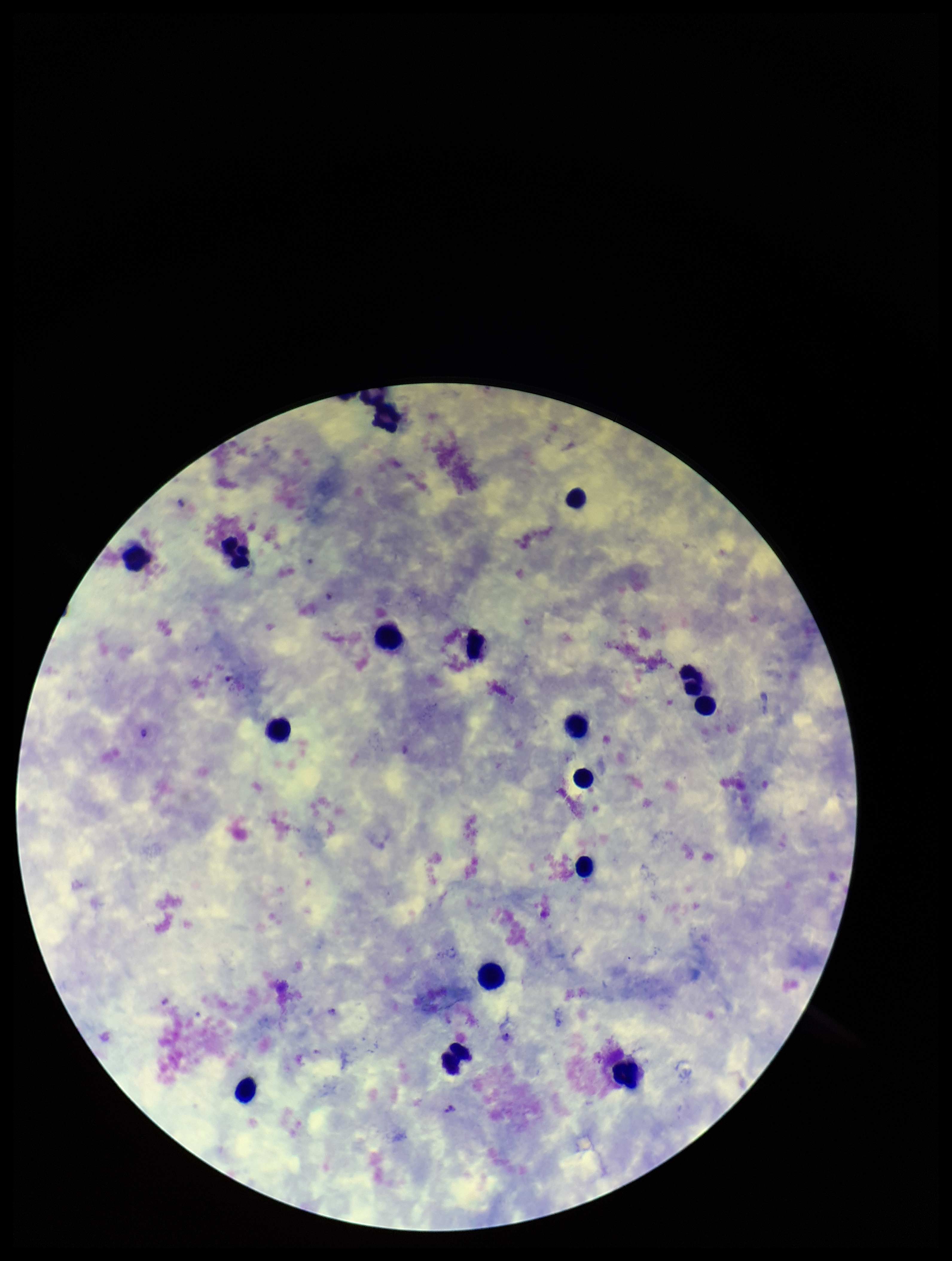
Summary:
  - Patient malaria status: infected
  - Parasite count: 6
  - Species reported for this patient: Plasmodium vivax
  - Field of view: single
  - Stain: Giemsa
  - Capture: smartphone photograph through the microscope eyepiece
  - Preparation: thick smear
  - Image size: 952×1261 pixels
  - Plasmodium parasites: identified
  - Leukocyte count: 16